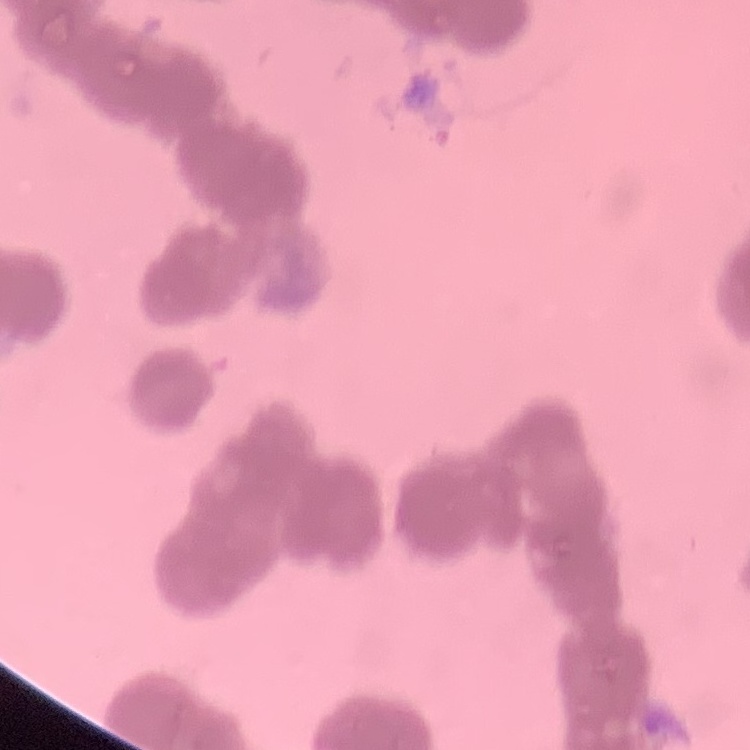
Summary:
  - Red blood cell morphology: rouleaux formation
  - Preparation: thin blood smear
  - Stain: Field's or Giemsa
  - Image type: square crop of a larger photomicrograph